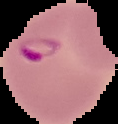

Summary:
  - Image type: cell region segmented out of the field of view; surrounding area masked to black
  - Image size: 118×124 pixels
  - Malaria status: parasitized
  - Preparation: thin blood smear